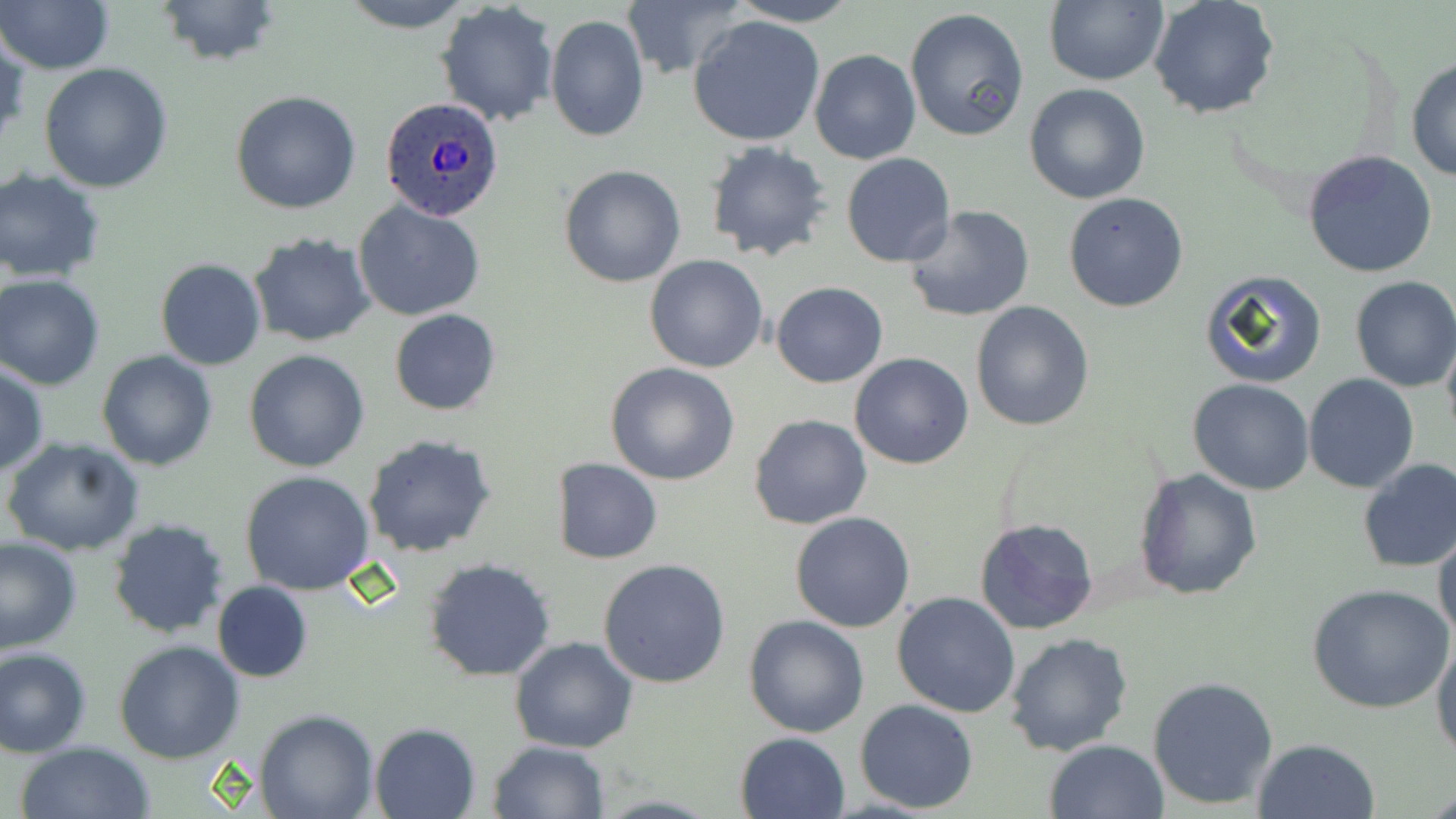 Approximate bounding boxes as (x1, y1, x2, y2) in pixels. Plasmodium ovale-infected red blood cell locations: (381, 96, 505, 221). Uninfected red blood cell locations: (0, 0, 117, 74), (154, 0, 281, 69), (335, 0, 478, 33), (722, 0, 864, 26), (1148, 0, 1281, 121), (617, 2, 745, 78), (1042, 2, 1168, 86), (436, 3, 560, 126), (906, 7, 1032, 144), (545, 14, 649, 142), (687, 14, 827, 147), (0, 32, 28, 149), (809, 48, 920, 164), (1404, 56, 1456, 184), (39, 64, 173, 193), (1023, 84, 1151, 205), (231, 90, 361, 213), (704, 141, 835, 264), (1300, 150, 1439, 279), (842, 153, 957, 269), (558, 163, 686, 288), (0, 170, 106, 282), (1062, 191, 1190, 313), (355, 201, 485, 320), (902, 204, 1035, 322), (250, 233, 377, 347), (644, 256, 768, 373), (155, 259, 267, 370), (1199, 269, 1327, 388), (1, 275, 108, 388), (1349, 277, 1456, 392), (771, 281, 887, 387), (970, 300, 1095, 432), (390, 308, 501, 415), (1441, 333, 1456, 447), (244, 348, 370, 472), (96, 350, 219, 472), (848, 351, 974, 468), (606, 362, 740, 485), (0, 365, 48, 476), (1303, 374, 1419, 493), (1189, 379, 1314, 496), (748, 413, 872, 530), (363, 433, 496, 557), (2, 436, 144, 557), (552, 457, 661, 565), (1356, 459, 1456, 573), (1132, 468, 1262, 599), (241, 471, 375, 594), (790, 511, 915, 633), (107, 518, 230, 639), (974, 518, 1100, 637), (1431, 528, 1456, 646), (0, 535, 82, 654), (424, 558, 555, 682), (598, 558, 731, 687), (212, 581, 312, 683), (1308, 583, 1453, 714), (891, 591, 1021, 718), (743, 614, 870, 737), (1004, 633, 1133, 757), (1431, 633, 1456, 763), (508, 635, 639, 754), (113, 639, 245, 763), (1, 646, 92, 756), (1147, 675, 1279, 810), (854, 699, 979, 814), (254, 710, 379, 819), (369, 722, 479, 819), (735, 732, 851, 819), (1251, 737, 1382, 819), (489, 739, 610, 819), (1043, 739, 1168, 819), (14, 741, 154, 819). Slide-level diagnosis: Plasmodium ovale. Thin blood film. 1000x magnification. May-Grünwald-Giemsa-stained preparation. One field of a larger specimen. Image is 1456×819 pixels. Light microscopy.